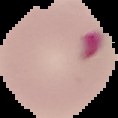

preparation = thin blood film
image size = 118×118 pixels
image type = cell region segmented out of the field of view; surrounding area masked to black
malaria status = parasitized